Classify this cell by malaria status.
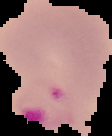
It is parasitized.

From a thin blood film. Cell region segmented out of the field of view; the surrounding area is masked to black. Image is 112×136 pixels.